State which parasite is depicted.
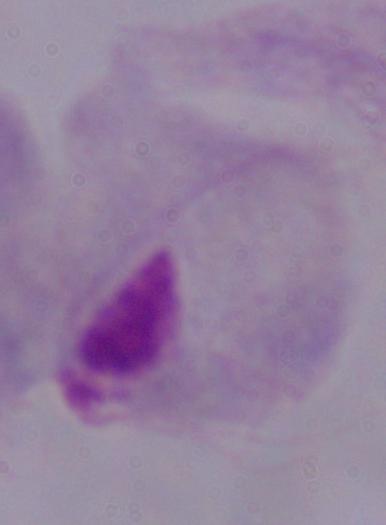

This is a trichomonad.

{
  "magnification": "1000x",
  "modality": "photomicrograph"
}